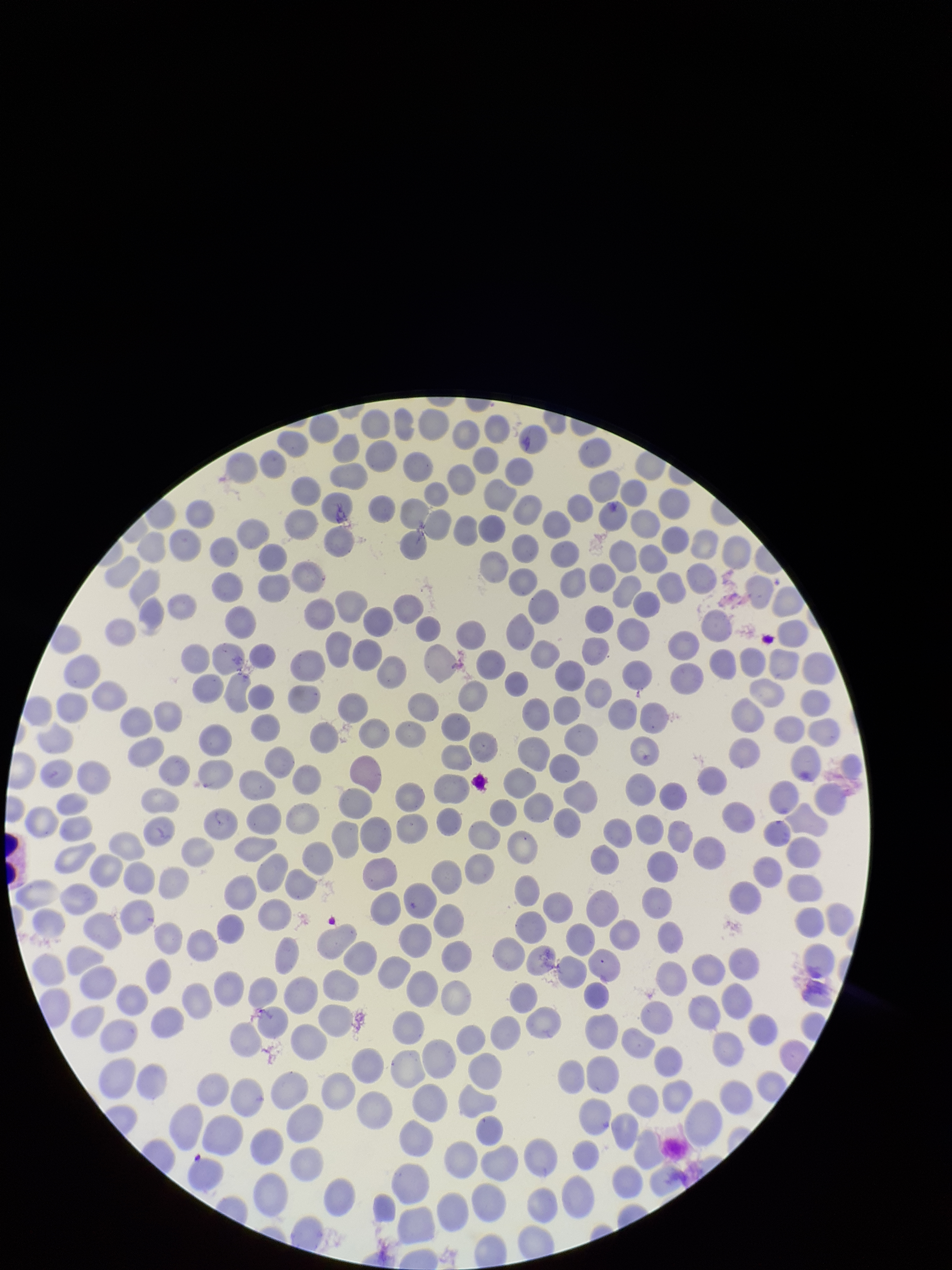 Parasitized red blood cells: none identified. Preparation: thin smear. One field from this slide. Photographed through the microscope eyepiece with a smartphone camera. Image is 952×1270 pixels. Giemsa stain. Patient malaria status: negative. Parasitized red blood cell count: 0. Red blood cell count: 327.